Name the parasite shown.
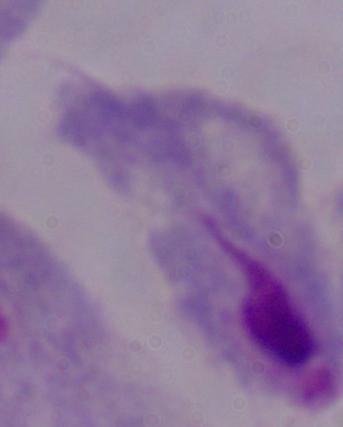

This is a trichomonad.

modality = micrograph
magnification = 1000x